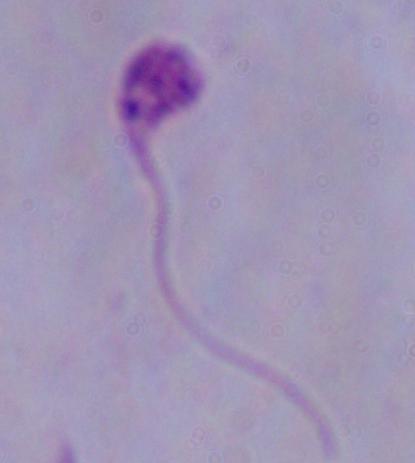
modality = micrograph
identification = Leishmania
magnification = 1000x